Classify this cell by malaria status.
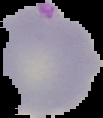
It is parasitized.

Summary:
  - Image type: segmented cell region with the area outside set to black
  - Image size: 103×118 pixels
  - Preparation: thin blood film